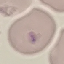
Summary:
  - Result: no malaria parasites seen
  - Capture: smartphone camera at the microscope eyepiece
  - Stain: Giemsa
  - Image type: automatically extracted cell patch, resized to 64 × 64 pixels
  - Preparation: thin blood smear